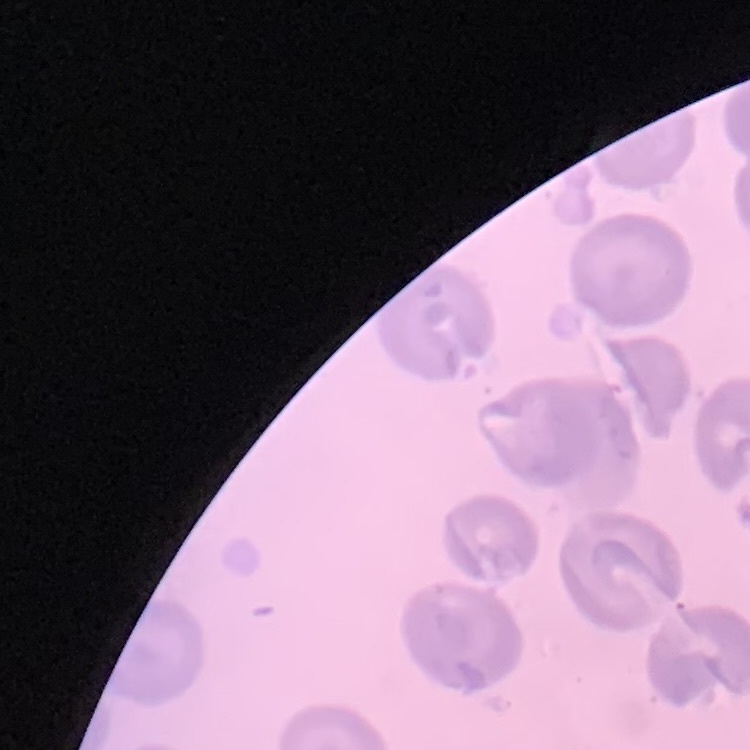

The erythrocytes show no rouleaux formation. Square crop of a larger photomicrograph. Thin blood film. Stained with either Field's or Giemsa.